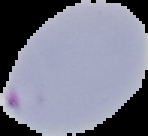
result = malaria parasites detected
image type = cell region segmented out of the field of view; surrounding area masked to black
preparation = thin blood smear
image size = 148×136 pixels